Report the malaria status of this cell.
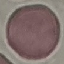
It is uninfected.

Summary:
  - Capture: smartphone camera at the microscope eyepiece
  - Preparation: thin blood smear
  - Stain: Giemsa
  - Image type: cell patch, automatically extracted from a larger field of view and resized to 64 × 64 pixels